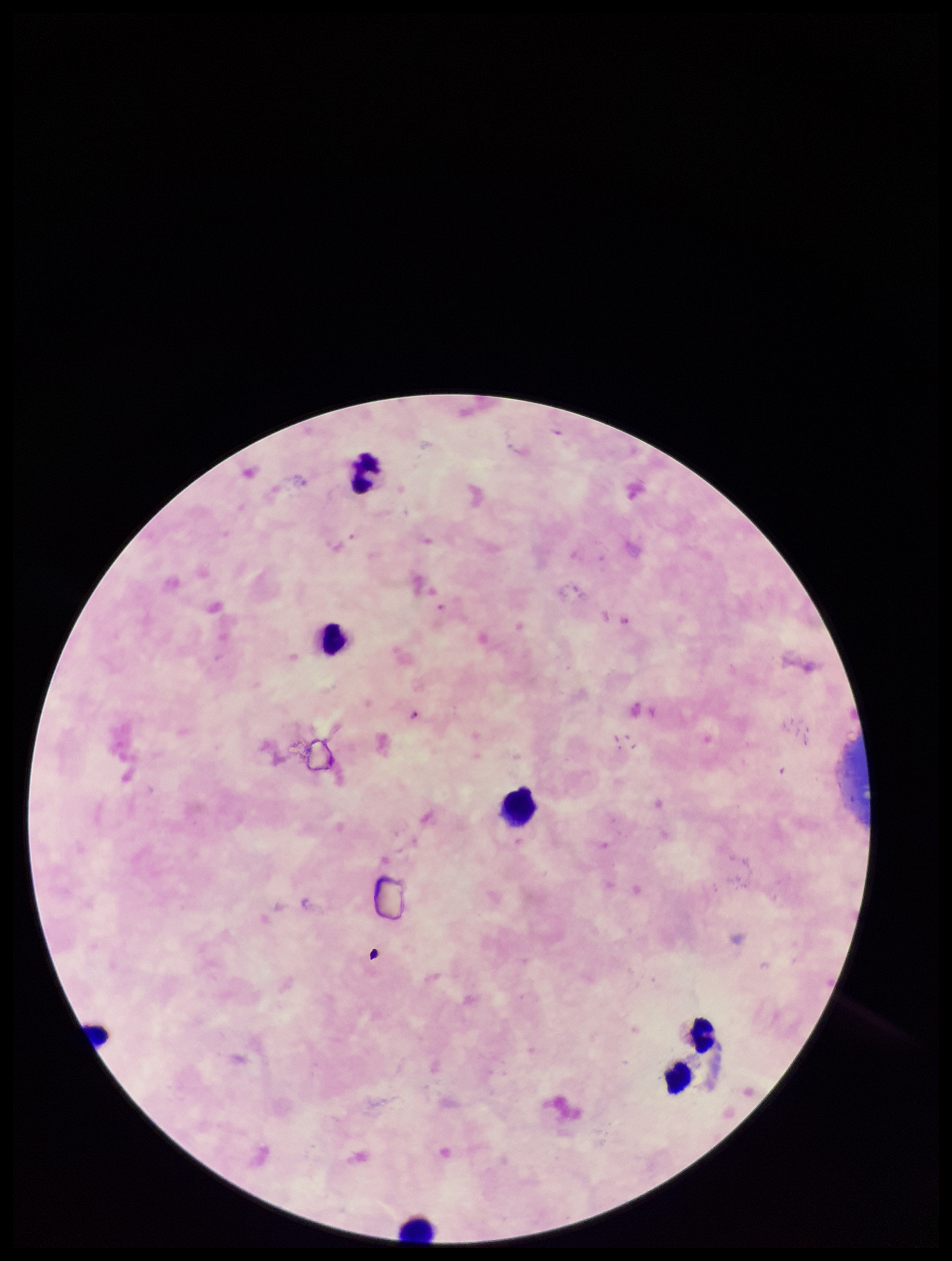
Summary:
  - Parasite count: 2
  - Capture: smartphone photograph through the microscope eyepiece
  - Leukocyte count: 7
  - Stain: Giemsa
  - Preparation: thick smear
  - Plasmodium parasites: detected
  - Species reported for this patient: Plasmodium falciparum
  - Patient malaria status: positive
  - Field of view: single
  - Image size: 952×1261 pixels